Describe the morphology of the red blood cells.
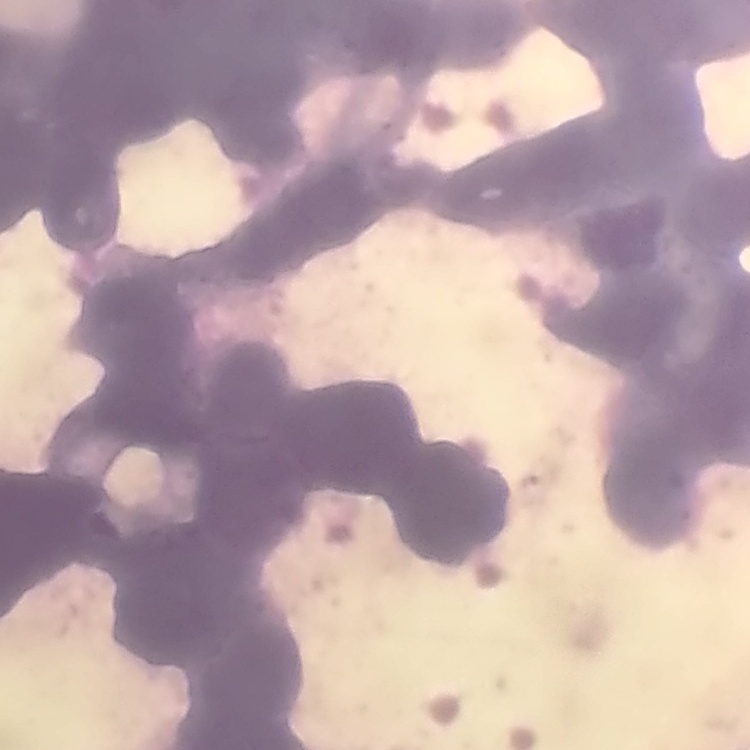

They show rouleaux formation.

image type = square crop of a larger photomicrograph
stain = Field's or Giemsa
preparation = thin peripheral smear